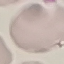
Summary:
  - Result: no malaria parasites detected
  - Image type: automatically extracted cell patch, resized to 64 × 64 pixels
  - Capture: smartphone camera at the microscope eyepiece
  - Preparation: thin blood smear
  - Stain: Giemsa